Name the cell type shown.
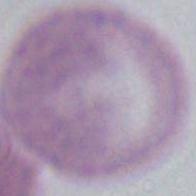
This is an erythrocyte.

magnification = 1000x
modality = micrograph